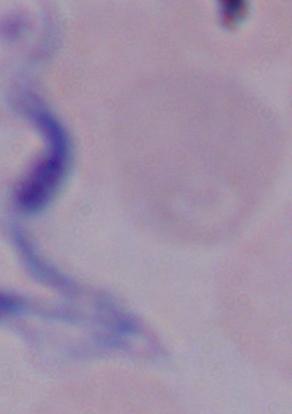
Summary:
  - Modality: photomicrograph
  - Magnification: 1000x
  - Identification: trypanosome